Assess this cell for malaria.
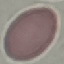
Uninfected.

{
  "image_type": "automatically extracted cell patch, resized to 64 × 64 pixels",
  "preparation": "thin blood film",
  "stain": "Giemsa",
  "capture": "smartphone through the microscope eyepiece"
}